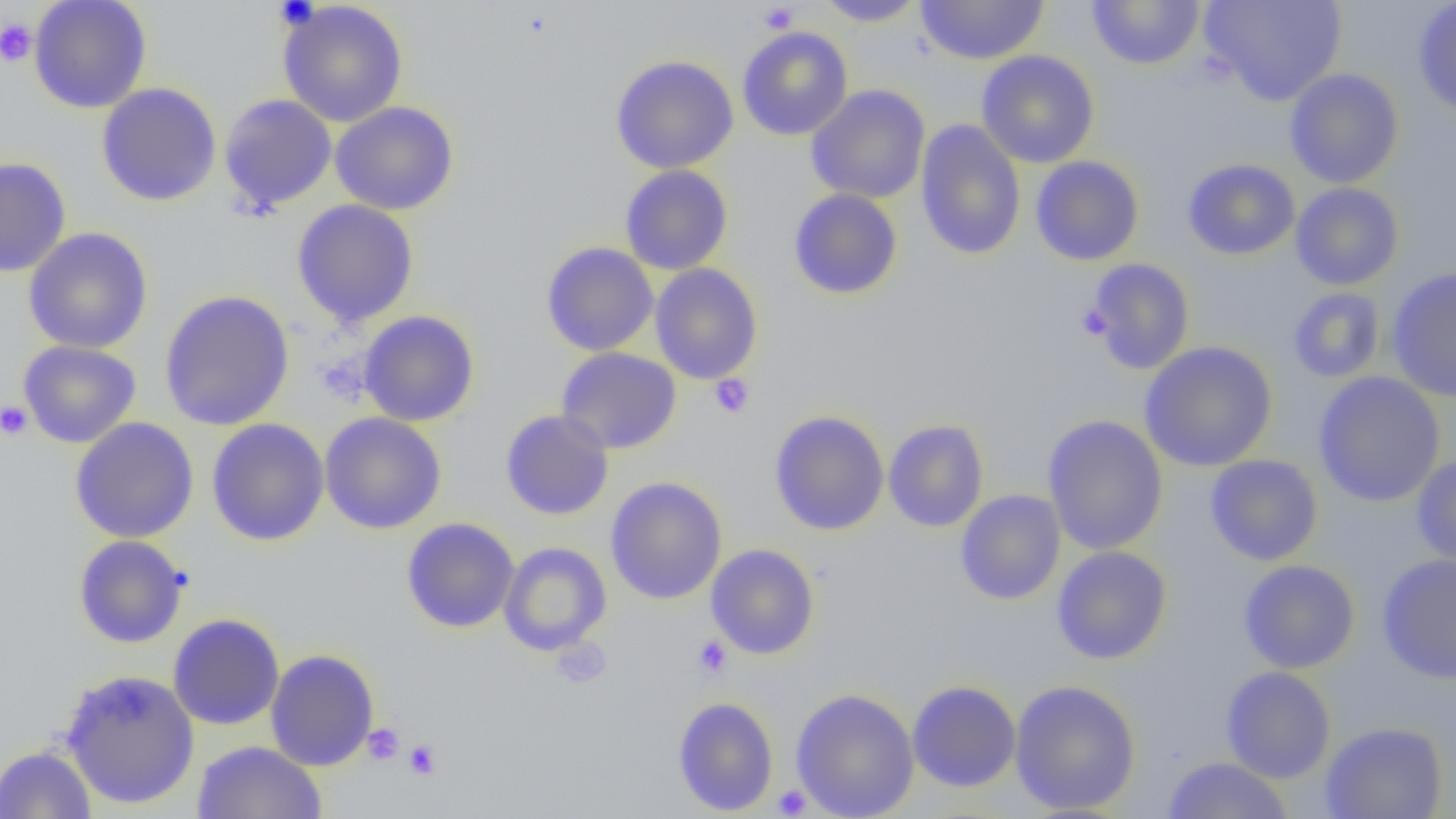
{
  "slide_level_diagnosis": "no evidence of blood parasites",
  "magnification": "1000x",
  "preparation": "thin blood film",
  "field_of_view": "one of a larger specimen",
  "modality": "light microscopy",
  "platelet_locations_subset": "approximate bounding boxes as (x1, y1, x2, y2) in pixels: (274, 0, 318, 28), (758, 3, 799, 33), (0, 18, 37, 67), (1077, 302, 1113, 340), (708, 374, 754, 418), (0, 401, 32, 440), (692, 635, 732, 679), (549, 637, 612, 689), (362, 723, 404, 766), (403, 739, 442, 780), (771, 785, 812, 817)",
  "uninfected_red_blood_cell_locations_subset": "approximate bounding boxes as (x1, y1, x2, y2) in pixels: (28, 0, 152, 114), (815, 0, 927, 26), (914, 0, 1050, 65), (1086, 0, 1206, 70), (1201, 0, 1346, 106), (1414, 0, 1456, 121), (278, 1, 408, 127), (737, 26, 853, 141), (977, 50, 1100, 168), (610, 54, 739, 174), (1285, 68, 1404, 189), (96, 83, 222, 206), (806, 85, 931, 204), (219, 93, 337, 213), (330, 101, 459, 215), (916, 119, 1026, 260), (0, 156, 71, 278), (1030, 156, 1144, 266), (1183, 158, 1301, 260), (620, 165, 733, 275), (1290, 183, 1404, 291), (788, 188, 903, 300), (292, 200, 419, 327), (23, 228, 153, 354), (541, 242, 658, 356), (650, 263, 763, 384), (1386, 267, 1456, 403), (1288, 288, 1386, 383), (159, 290, 294, 431), (358, 310, 480, 427), (18, 340, 141, 448), (1139, 341, 1278, 471), (556, 347, 682, 454), (1314, 372, 1446, 508), (500, 409, 614, 520), (770, 410, 889, 535), (320, 412, 447, 534), (1043, 414, 1168, 556), (70, 417, 200, 543), (206, 418, 330, 546), (883, 419, 989, 532), (1205, 454, 1323, 566), (1412, 454, 1456, 568), (606, 477, 727, 604), (955, 490, 1066, 605), (402, 517, 519, 633), (73, 535, 189, 648), (499, 542, 612, 655), (706, 543, 820, 659), (1051, 546, 1172, 665), (1377, 553, 1456, 684), (1239, 559, 1360, 674), (168, 613, 284, 730), (265, 649, 379, 771), (1221, 666, 1336, 783), (59, 668, 200, 809), (907, 679, 1021, 792), (1009, 679, 1141, 815), (790, 688, 920, 819), (673, 696, 779, 816), (1320, 721, 1448, 819), (191, 740, 327, 818), (0, 744, 96, 818), (1162, 756, 1294, 818)",
  "image_size": "1456×819 pixels"
}